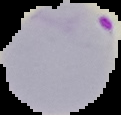

From a thin blood smear. Image is 121×115 pixels. The area outside the segmented cell region is set to black. Malaria status: parasitized.